Describe the morphology of the red blood cells.
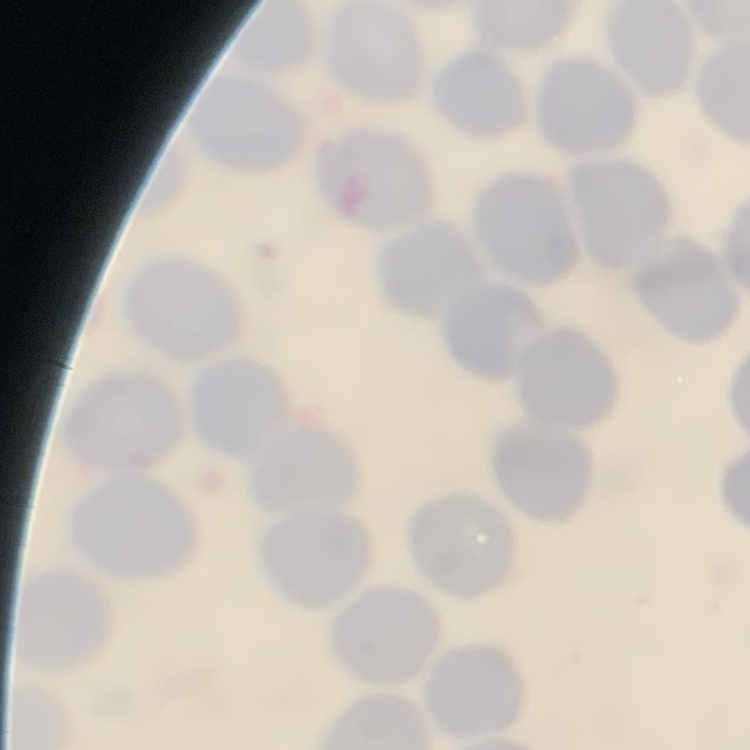
No rouleaux formation.

Stained with either Field's or Giemsa. Square crop of a larger photomicrograph. Thin peripheral smear.